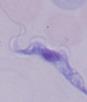

Summary:
  - Identification: trypanosome
  - Magnification: 1000x
  - Modality: photomicrograph